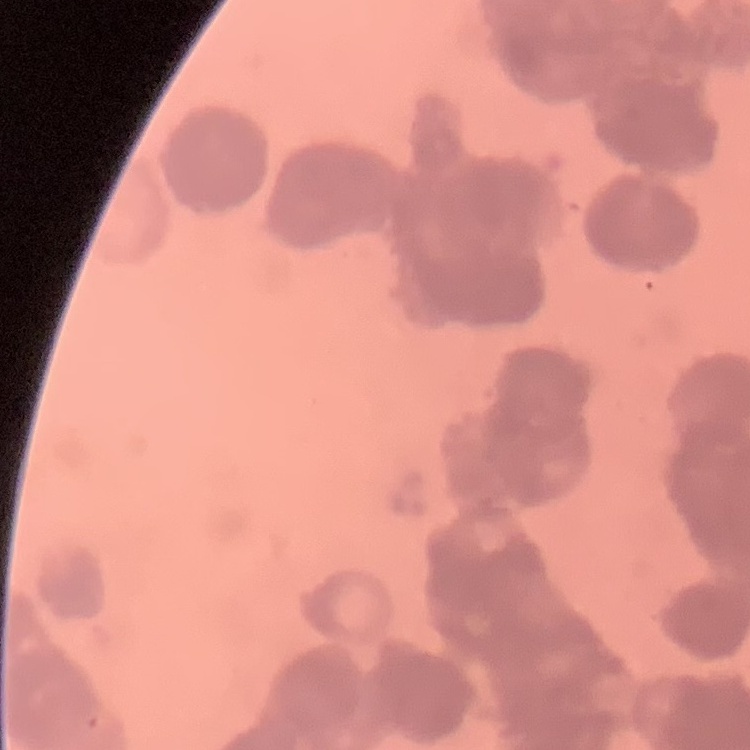

The erythrocytes exhibit rouleaux formation. Thin blood smear. Square crop of a larger photomicrograph. Stained with either Field's or Giemsa.